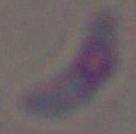 Toxoplasma gondii is seen. Captured at 1000x magnification. Micrograph.